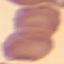
result: no malaria parasites detected
stain: Giemsa
image_type: automatically extracted cell patch, resized to 64 × 64 pixels
capture: smartphone through the microscope eyepiece
preparation: thin blood film